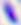

modality = micrograph
magnification = 400x
identification = Toxoplasma gondii